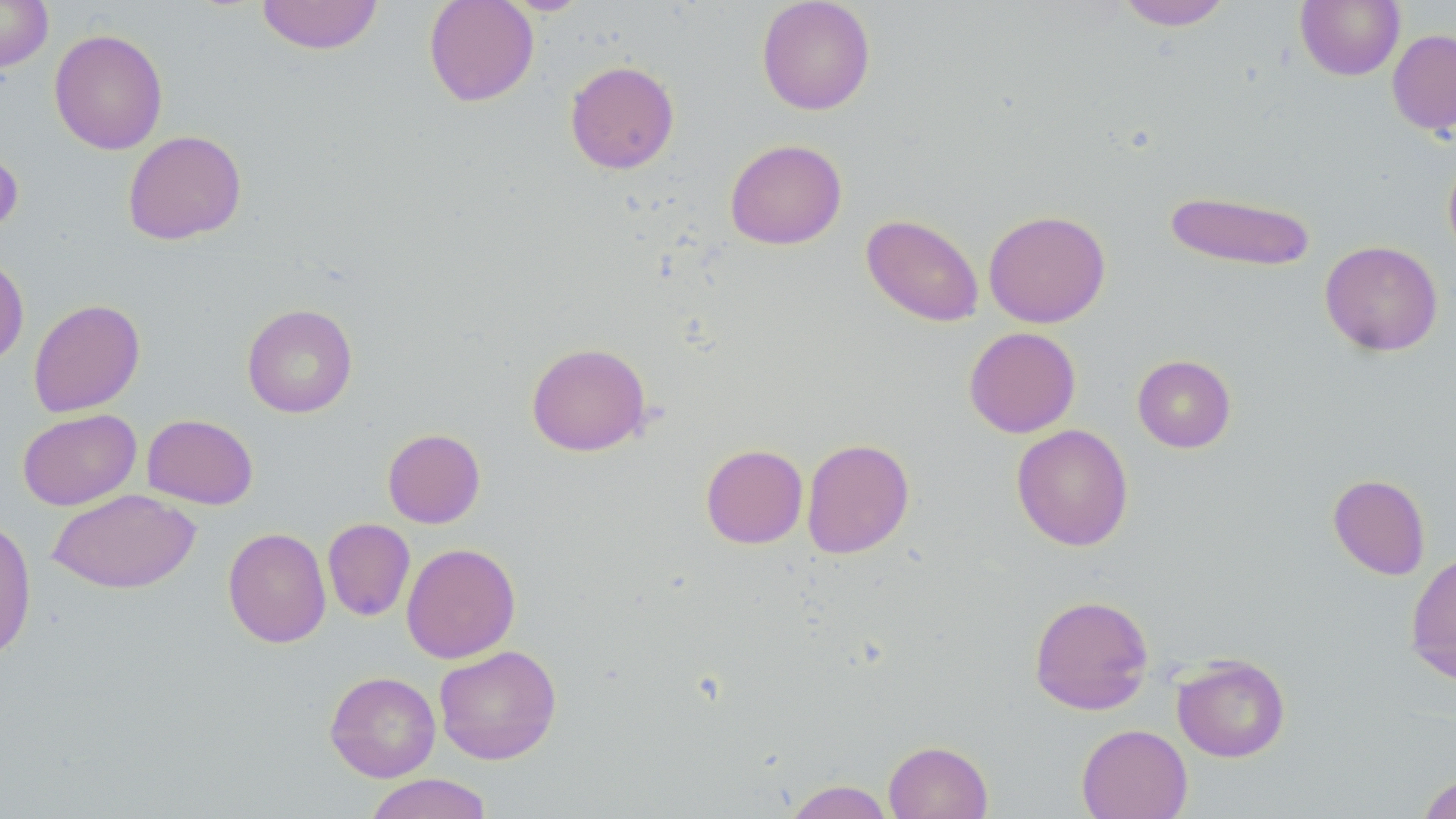
Summary:
  - Coordinate format: approximate bounding boxes as (x1, y1, x2, y2) in pixels
  - Uninfected red blood cell locations: (0, 0, 53, 71), (256, 0, 384, 55), (423, 0, 539, 107), (756, 0, 876, 115), (1116, 0, 1233, 31), (1295, 0, 1405, 80), (49, 29, 168, 155), (1387, 29, 1456, 135), (565, 60, 680, 174), (123, 130, 247, 245), (0, 136, 24, 237), (724, 138, 847, 250), (1443, 149, 1456, 261), (1164, 190, 1317, 271), (983, 209, 1111, 328), (861, 213, 984, 327), (1319, 240, 1443, 356), (0, 254, 29, 366), (28, 299, 145, 417), (242, 303, 358, 418), (964, 326, 1081, 438), (526, 342, 651, 456), (1132, 354, 1236, 453), (17, 408, 141, 511), (142, 414, 258, 510), (1011, 424, 1133, 551), (383, 428, 485, 528), (802, 438, 914, 559), (701, 444, 808, 548), (1328, 474, 1430, 580), (48, 489, 200, 594), (0, 515, 37, 664), (323, 518, 415, 621), (222, 527, 331, 648), (401, 542, 521, 663), (1405, 550, 1456, 686), (1028, 593, 1154, 715), (434, 645, 562, 764), (1173, 654, 1290, 763), (325, 671, 441, 782), (1076, 724, 1193, 819), (883, 740, 993, 819), (1415, 772, 1456, 818), (363, 773, 494, 819), (783, 779, 894, 819)
  - Slide-level diagnosis: negative for blood parasites
  - Stain: May-Grünwald-Giemsa
  - Image size: 1456×819 pixels
  - Preparation: thin blood film
  - Magnification: 1000x
  - Field of view: single
  - Modality: optical microscopy